Identify the blood parasite species.
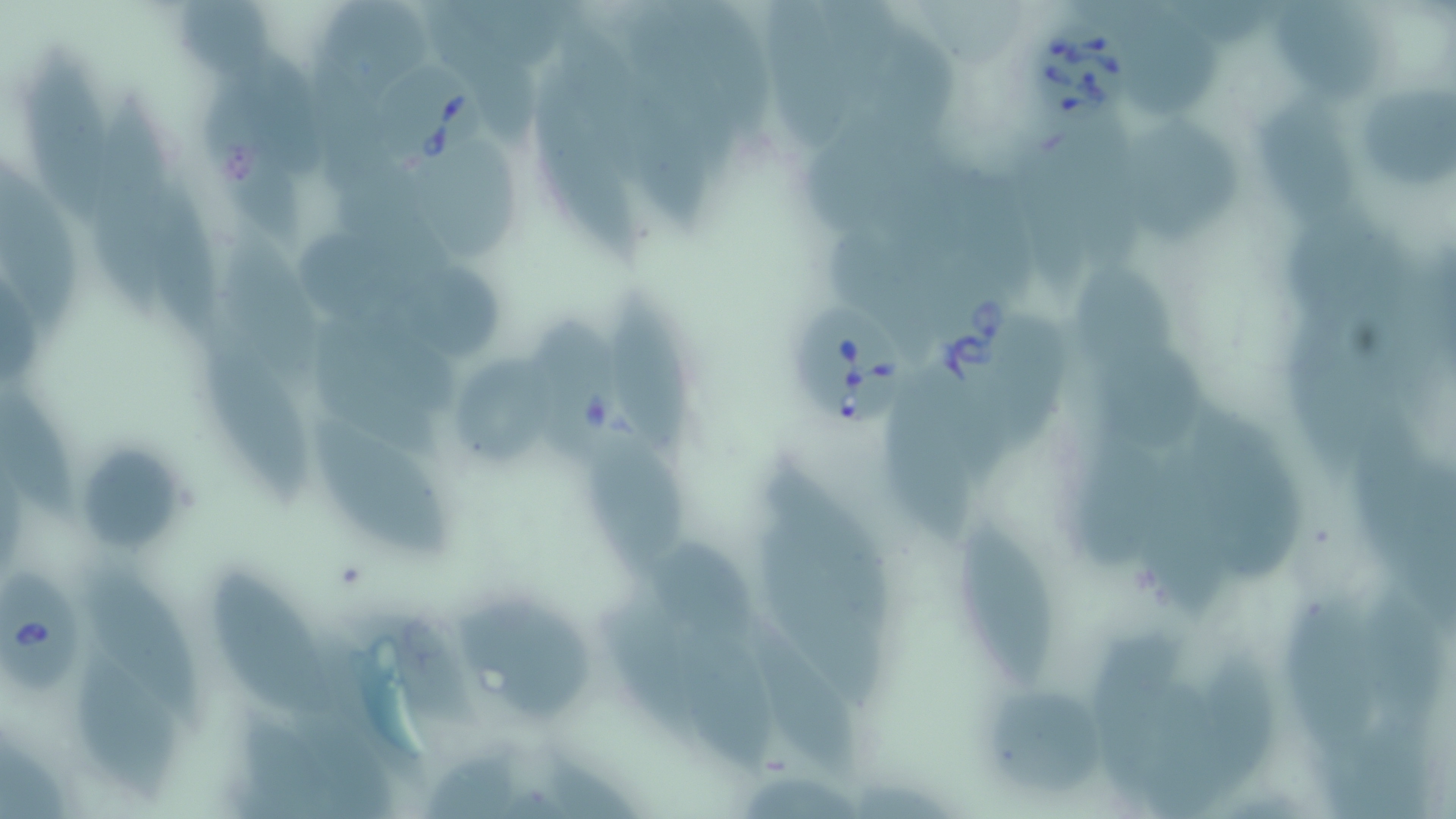
Babesia divergens.

Approximate bounding boxes as named x1/y1/x2/y2 corners in pixels. Babesia divergens-infected red blood cell locations: (x1=1028, y1=20, x2=1134, y2=131), (x1=369, y1=53, x2=494, y2=169), (x1=924, y1=285, x2=1034, y2=406), (x1=791, y1=299, x2=906, y2=427), (x1=526, y1=311, x2=625, y2=473), (x1=0, y1=566, x2=94, y2=700). Uninfected red blood cell locations: (x1=322, y1=2, x2=439, y2=100), (x1=1115, y1=2, x2=1229, y2=121), (x1=1272, y1=2, x2=1389, y2=103), (x1=765, y1=5, x2=859, y2=158), (x1=25, y1=56, x2=109, y2=229), (x1=612, y1=56, x2=714, y2=234), (x1=528, y1=75, x2=650, y2=275), (x1=1359, y1=80, x2=1456, y2=192), (x1=203, y1=82, x2=306, y2=248), (x1=88, y1=84, x2=175, y2=319), (x1=1251, y1=99, x2=1362, y2=235), (x1=1129, y1=115, x2=1241, y2=252), (x1=414, y1=146, x2=522, y2=264), (x1=0, y1=160, x2=83, y2=342), (x1=151, y1=170, x2=221, y2=351), (x1=298, y1=227, x2=428, y2=321), (x1=218, y1=230, x2=327, y2=381), (x1=1081, y1=264, x2=1185, y2=386), (x1=375, y1=267, x2=504, y2=362), (x1=606, y1=288, x2=700, y2=464), (x1=199, y1=332, x2=312, y2=505), (x1=1093, y1=346, x2=1213, y2=456), (x1=453, y1=359, x2=560, y2=467), (x1=0, y1=376, x2=77, y2=522), (x1=887, y1=381, x2=979, y2=550), (x1=1186, y1=402, x2=1308, y2=582), (x1=307, y1=418, x2=455, y2=560), (x1=585, y1=426, x2=687, y2=581), (x1=79, y1=446, x2=184, y2=551), (x1=960, y1=523, x2=1055, y2=690), (x1=757, y1=527, x2=883, y2=715), (x1=652, y1=536, x2=768, y2=645), (x1=82, y1=568, x2=202, y2=734), (x1=208, y1=568, x2=344, y2=720), (x1=449, y1=591, x2=593, y2=717), (x1=607, y1=596, x2=712, y2=737), (x1=1286, y1=599, x2=1381, y2=760), (x1=680, y1=622, x2=780, y2=780), (x1=1087, y1=625, x2=1188, y2=803), (x1=71, y1=646, x2=178, y2=804), (x1=1184, y1=653, x2=1280, y2=804), (x1=981, y1=684, x2=1106, y2=800). May-Grünwald-Giemsa-stained preparation. One field of a larger specimen. Image is 1456×819 pixels. Thin blood smear. Captured at 1000x magnification. Light microscopy.